Find each parasitized red blood cell.
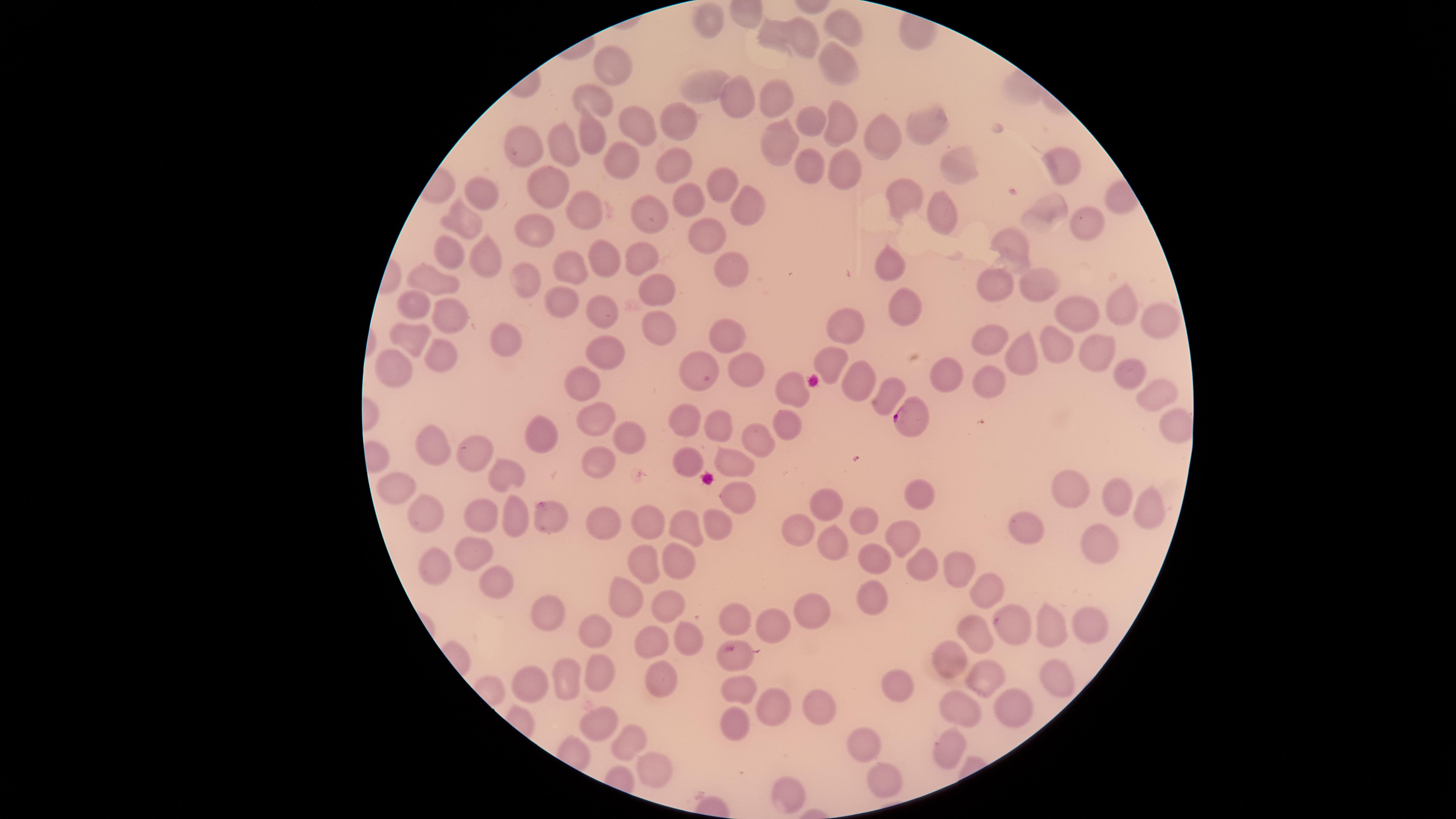
Approximate marker points as {x, y} in pixels.
Parasitized red blood cells: {906, 418}, {735, 653}.

Approximate marker points as {x, y} in pixels. Uninfected red blood cells: {708, 22}, {841, 23}, {767, 30}, {806, 40}, {835, 63}, {608, 66}, {706, 87}, {774, 98}, {597, 101}, {736, 101}, {812, 119}, {921, 121}, {683, 123}, {633, 124}, {841, 124}, {779, 141}, {883, 143}, {583, 144}, {526, 154}, {564, 154}, {676, 164}, {1061, 164}, {626, 168}, {805, 168}, {948, 168}, {835, 169}, {717, 177}, {548, 182}, {483, 194}, {901, 200}, {744, 204}, {1048, 209}, {689, 210}, {648, 212}, {939, 212}, {579, 213}, {456, 219}, {1081, 221}, {529, 228}, {704, 232}, {1015, 248}, {481, 253}, {641, 253}, {448, 256}, {603, 259}, {731, 263}, {572, 266}, {890, 266}, {435, 273}, {522, 279}, {1001, 280}, {1029, 280}, {658, 290}, {554, 299}, {411, 301}, {1119, 305}, {911, 307}, {598, 308}, {443, 309}, {1082, 318}, {1147, 323}, {729, 327}, {847, 328}, {657, 333}, {412, 339}, {989, 340}, {1055, 344}, {1090, 345}, {491, 346}, {604, 348}, {1017, 349}, {439, 355}, {826, 361}, {390, 366}, {697, 367}, {746, 372}, {1126, 373}, {947, 376}, {580, 382}, {858, 383}, {984, 386}, {789, 390}, {1153, 393}, {883, 395}, {596, 419}, {686, 420}, {781, 425}, {718, 426}, {620, 437}, {544, 439}, {760, 439}, {428, 444}, {479, 451}, {684, 458}, {730, 461}, {596, 465}, {504, 470}, {394, 487}, {1077, 489}, {922, 493}, {1115, 496}, {733, 497}, {829, 505}, {1134, 508}, {420, 514}, {543, 516}, {647, 519}, {870, 519}, {477, 522}, {601, 523}, {1033, 524}, {799, 525}, {683, 526}, {711, 526}, {900, 537}, {1094, 539}, {833, 542}, {466, 549}, {878, 559}, {673, 561}, {641, 563}, {915, 565}, {954, 565}, {428, 570}, {489, 586}, {991, 591}, {616, 593}, {867, 594}, {812, 598}, {550, 608}, {665, 609}, {739, 615}, {1020, 622}, {778, 624}, {976, 626}, {1049, 626}, {602, 629}, {1090, 631}, {683, 640}, {654, 643}, {953, 655}, {556, 670}, {595, 671}, {1053, 678}, {659, 680}, {979, 681}, {527, 683}, {736, 683}, {900, 686}, {1011, 705}, {768, 706}, {958, 708}, {821, 712}, {730, 716}, {598, 721}, {867, 742}, {942, 746}, {623, 748}, {882, 776}, {649, 777}, {788, 786}. One field of view of the specimen. Circular visible region. Photographed with a smartphone camera through the microscope eyepiece. Species: Plasmodium falciparum. Giemsa stain. Image is 1456×819 pixels. Thin blood film.